Classify this cell by malaria status.
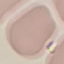
It is uninfected.

capture = smartphone through the microscope eyepiece
stain = Giemsa
image type = automatically extracted cell patch, resized to 64 × 64 pixels
preparation = thin smear